Give the extent of all Plasmodium falciparum-infected red blood cells.
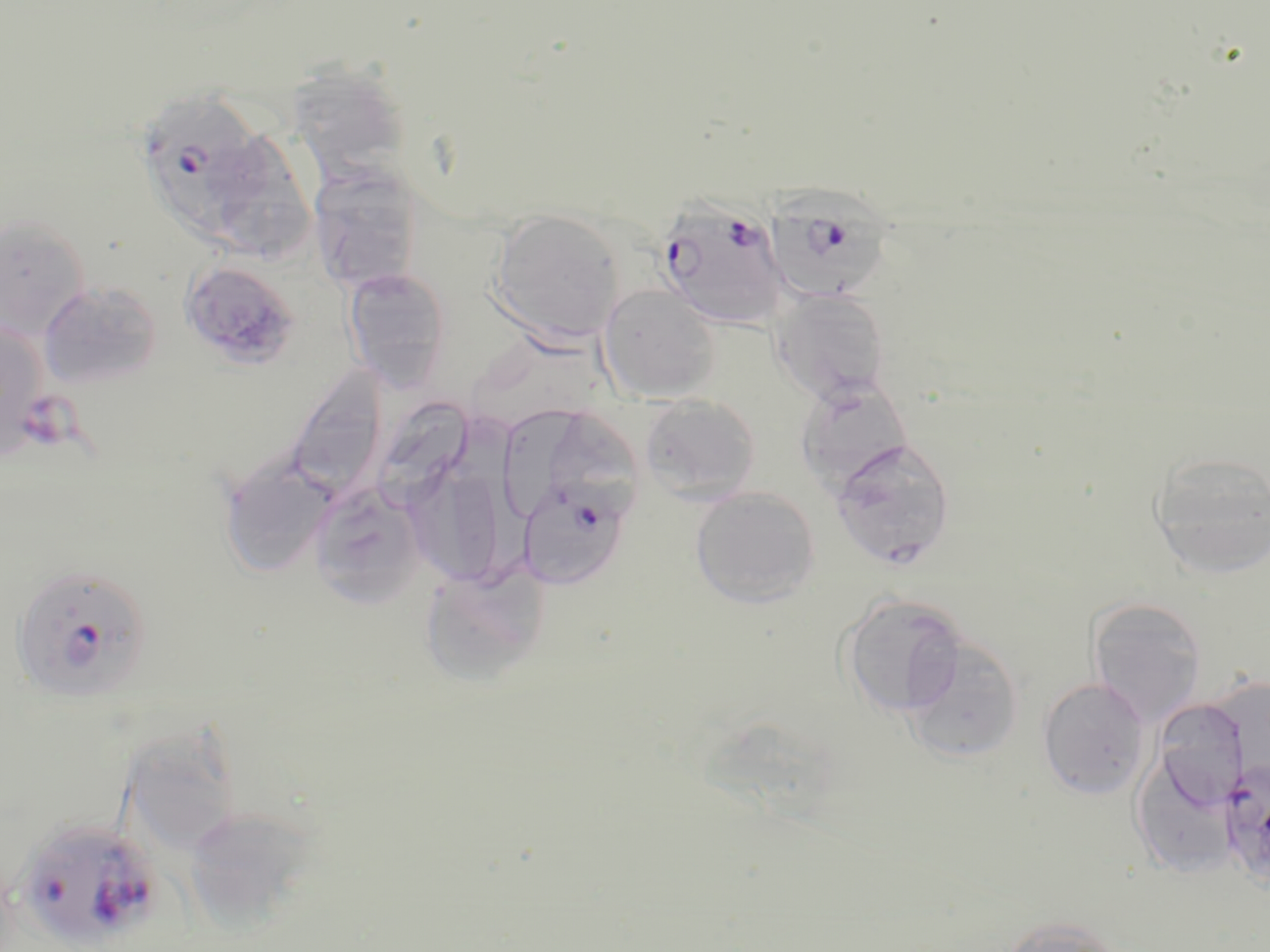

Approximate bounding boxes as named x1/y1/x2/y2 corners in pixels.
Plasmodium falciparum-infected red blood cells: (x1=131, y1=86, x2=270, y2=241), (x1=766, y1=195, x2=895, y2=304), (x1=661, y1=196, x2=795, y2=327), (x1=517, y1=476, x2=631, y2=589), (x1=11, y1=563, x2=152, y2=703), (x1=1219, y1=762, x2=1270, y2=893), (x1=13, y1=818, x2=163, y2=950).

slide-level diagnosis = Plasmodium falciparum
modality = optical microscopy
stain = May-Grünwald-Giemsa
preparation = thin blood smear
field of view = one of a larger specimen
image size = 1270×952 pixels
magnification = 1000x
uninfected red blood cell locations = approximate bounding boxes as named x1/y1/x2/y2 corners in pixels: (x1=287, y1=64, x2=411, y2=180), (x1=199, y1=124, x2=318, y2=263), (x1=308, y1=164, x2=424, y2=294), (x1=488, y1=209, x2=626, y2=344), (x1=0, y1=213, x2=90, y2=340), (x1=179, y1=260, x2=301, y2=369), (x1=342, y1=267, x2=452, y2=391), (x1=38, y1=281, x2=163, y2=388), (x1=598, y1=283, x2=722, y2=404), (x1=771, y1=288, x2=892, y2=404), (x1=0, y1=316, x2=50, y2=457), (x1=285, y1=365, x2=390, y2=500), (x1=795, y1=379, x2=915, y2=493), (x1=640, y1=393, x2=761, y2=502), (x1=374, y1=401, x2=469, y2=507), (x1=505, y1=403, x2=606, y2=519), (x1=444, y1=404, x2=547, y2=583), (x1=830, y1=438, x2=956, y2=569), (x1=1149, y1=451, x2=1270, y2=579), (x1=217, y1=455, x2=337, y2=578), (x1=412, y1=476, x2=504, y2=585), (x1=308, y1=480, x2=428, y2=608), (x1=689, y1=487, x2=821, y2=608), (x1=418, y1=561, x2=550, y2=688), (x1=839, y1=593, x2=968, y2=717), (x1=1086, y1=597, x2=1207, y2=726), (x1=898, y1=634, x2=1024, y2=764), (x1=1037, y1=677, x2=1151, y2=800), (x1=1165, y1=704, x2=1247, y2=808), (x1=112, y1=720, x2=238, y2=853), (x1=1130, y1=755, x2=1239, y2=878), (x1=183, y1=806, x2=316, y2=929), (x1=999, y1=916, x2=1128, y2=952)